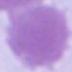

identification = red blood cell
modality = photomicrograph
magnification = 1000x